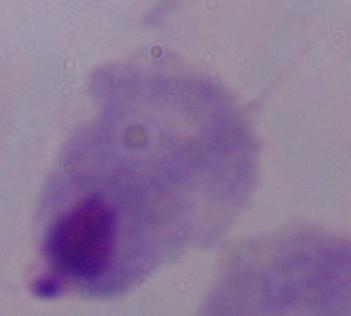 A trichomonad is shown. Photomicrograph. Captured at 1000x magnification.